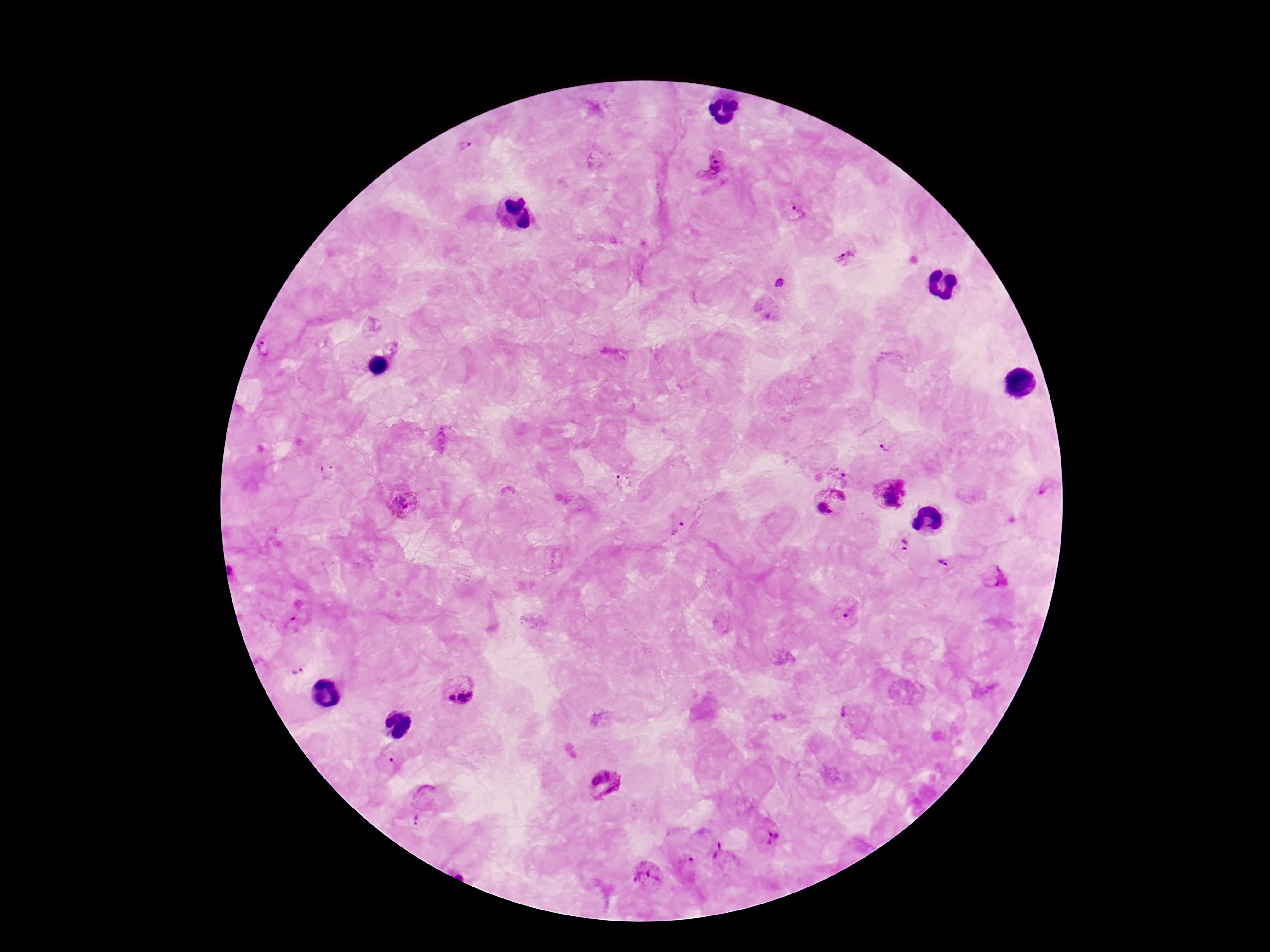

Approximate object centers, in pixels from the top-left corner.
Summary:
  - Plasmodium parasite locations: (x=464, y=146), (x=712, y=167), (x=797, y=211), (x=846, y=257), (x=779, y=282), (x=265, y=348), (x=441, y=439), (x=884, y=445), (x=839, y=471), (x=327, y=473), (x=622, y=482), (x=891, y=494), (x=402, y=502), (x=830, y=502), (x=679, y=529), (x=905, y=544), (x=945, y=564), (x=996, y=578), (x=850, y=611), (x=293, y=624), (x=297, y=670), (x=459, y=691), (x=392, y=760), (x=605, y=783), (x=425, y=796), (x=415, y=820), (x=768, y=835), (x=724, y=860), (x=688, y=865), (x=646, y=876)
  - Capture: smartphone camera through the microscope eyepiece
  - Image size: 1270×952 pixels
  - Field of view: single
  - Patient malaria status: infected
  - Magnification: 100x
  - Preparation: thick blood film
  - Stain: Giemsa